Locate every Plasmodium parasite.
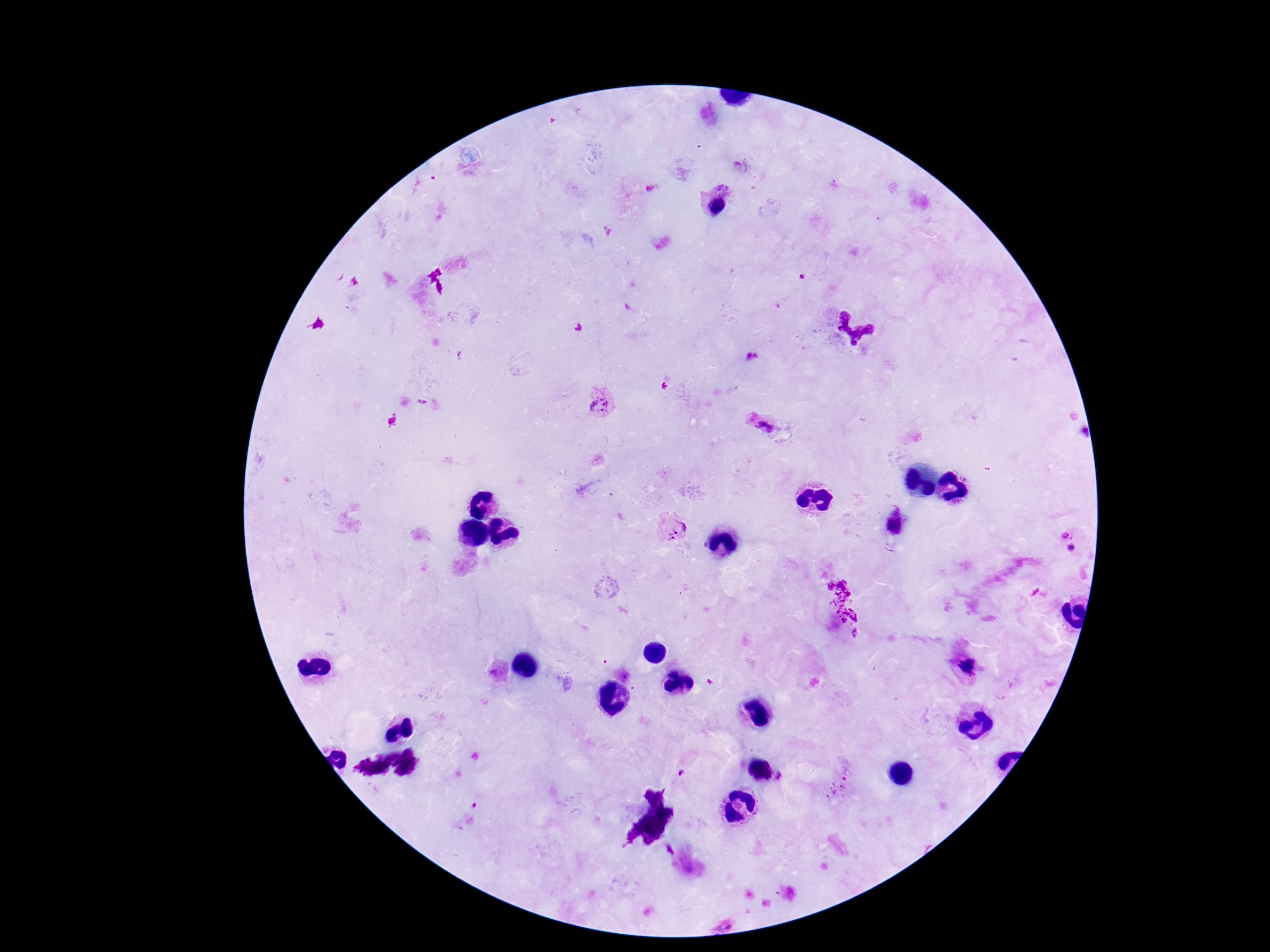

Approximate centers as [x, y] in pixels.
Plasmodium parasites: [724, 187], [717, 207], [600, 403], [763, 423], [683, 523], [894, 524], [1065, 534], [671, 536], [1071, 548], [967, 666].

Summary:
  - Capture: smartphone camera through the microscope eyepiece
  - Magnification: 100x
  - Stain: Giemsa
  - Field of view: single
  - Patient malaria status: positive
  - Image size: 1270×952 pixels
  - Preparation: thick peripheral-blood smear